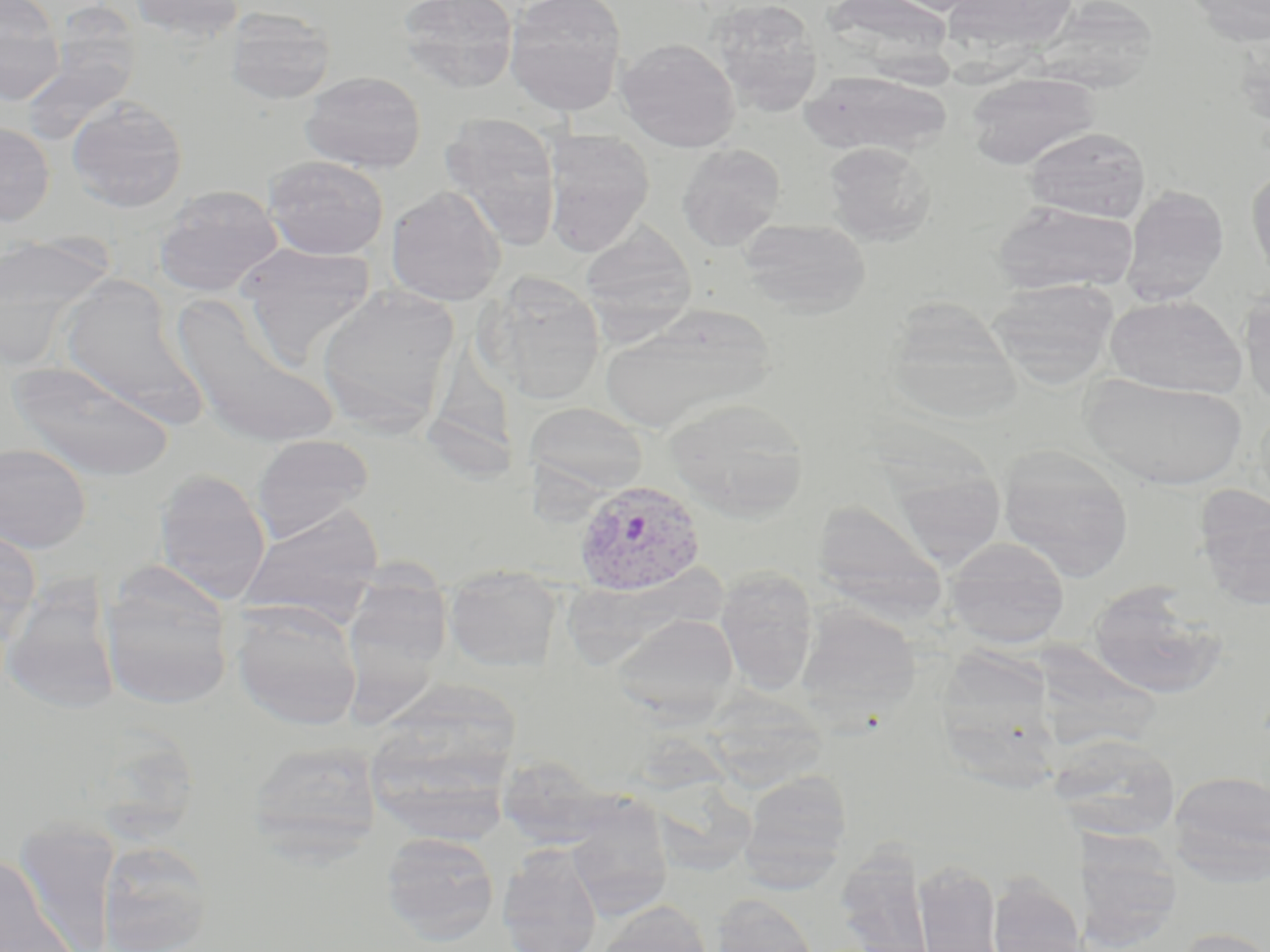
slide-level diagnosis = Plasmodium vivax
preparation = thin blood film
uninfected red blood cell locations = approximate bounding boxes as named x1/y1/x2/y2 corners in pixels: (x1=127, y1=0, x2=246, y2=41), (x1=396, y1=0, x2=519, y2=93), (x1=505, y1=0, x2=627, y2=115), (x1=710, y1=0, x2=823, y2=116), (x1=821, y1=0, x2=956, y2=72), (x1=942, y1=0, x2=1077, y2=53), (x1=1184, y1=0, x2=1270, y2=45), (x1=1034, y1=3, x2=1159, y2=92), (x1=224, y1=8, x2=336, y2=105), (x1=0, y1=11, x2=64, y2=106), (x1=20, y1=29, x2=141, y2=145), (x1=1232, y1=30, x2=1270, y2=133), (x1=616, y1=38, x2=740, y2=152), (x1=801, y1=70, x2=950, y2=156), (x1=301, y1=71, x2=425, y2=173), (x1=966, y1=72, x2=1099, y2=170), (x1=66, y1=96, x2=188, y2=212), (x1=440, y1=114, x2=563, y2=250), (x1=0, y1=123, x2=55, y2=225), (x1=1024, y1=126, x2=1151, y2=222), (x1=541, y1=130, x2=655, y2=255), (x1=824, y1=142, x2=934, y2=245), (x1=677, y1=144, x2=785, y2=250), (x1=263, y1=156, x2=389, y2=260), (x1=1246, y1=167, x2=1270, y2=286), (x1=153, y1=185, x2=283, y2=297), (x1=386, y1=185, x2=506, y2=306), (x1=1120, y1=185, x2=1229, y2=306), (x1=993, y1=201, x2=1139, y2=295), (x1=739, y1=218, x2=871, y2=316), (x1=580, y1=223, x2=697, y2=332), (x1=0, y1=231, x2=111, y2=349), (x1=238, y1=243, x2=377, y2=362), (x1=483, y1=277, x2=606, y2=405), (x1=986, y1=278, x2=1120, y2=387), (x1=57, y1=281, x2=204, y2=423), (x1=316, y1=284, x2=460, y2=434), (x1=1239, y1=289, x2=1270, y2=410), (x1=170, y1=292, x2=338, y2=450), (x1=1104, y1=295, x2=1246, y2=398), (x1=600, y1=305, x2=773, y2=434), (x1=901, y1=306, x2=1027, y2=431), (x1=429, y1=349, x2=527, y2=501), (x1=6, y1=358, x2=175, y2=481), (x1=1084, y1=375, x2=1247, y2=488), (x1=666, y1=396, x2=810, y2=520), (x1=524, y1=402, x2=648, y2=497), (x1=251, y1=435, x2=374, y2=542), (x1=0, y1=442, x2=92, y2=553), (x1=998, y1=445, x2=1135, y2=581), (x1=887, y1=459, x2=1007, y2=572), (x1=153, y1=468, x2=271, y2=603), (x1=1194, y1=487, x2=1270, y2=610), (x1=814, y1=501, x2=947, y2=617), (x1=238, y1=504, x2=384, y2=625), (x1=0, y1=527, x2=41, y2=651), (x1=943, y1=537, x2=1070, y2=648), (x1=352, y1=556, x2=458, y2=725), (x1=444, y1=565, x2=562, y2=672), (x1=715, y1=567, x2=819, y2=694), (x1=99, y1=570, x2=234, y2=711), (x1=2, y1=581, x2=119, y2=714), (x1=1087, y1=581, x2=1227, y2=700), (x1=230, y1=600, x2=363, y2=730), (x1=797, y1=604, x2=920, y2=723), (x1=610, y1=611, x2=739, y2=720), (x1=941, y1=639, x2=1059, y2=794), (x1=378, y1=677, x2=532, y2=841), (x1=713, y1=689, x2=833, y2=795), (x1=1048, y1=733, x2=1182, y2=841), (x1=247, y1=739, x2=383, y2=858), (x1=495, y1=757, x2=627, y2=850), (x1=738, y1=769, x2=854, y2=887), (x1=1168, y1=769, x2=1270, y2=884), (x1=566, y1=811, x2=672, y2=919), (x1=12, y1=822, x2=122, y2=951), (x1=1080, y1=828, x2=1182, y2=949), (x1=380, y1=831, x2=500, y2=946), (x1=95, y1=840, x2=216, y2=952), (x1=497, y1=844, x2=603, y2=952), (x1=836, y1=850, x2=936, y2=952), (x1=0, y1=854, x2=75, y2=952), (x1=914, y1=859, x2=1003, y2=952), (x1=987, y1=873, x2=1084, y2=952), (x1=709, y1=892, x2=821, y2=952), (x1=596, y1=900, x2=714, y2=952), (x1=1172, y1=926, x2=1270, y2=952)
image size = 1270×952 pixels
field of view = one of a larger specimen
Plasmodium vivax-infected red blood cell locations = approximate bounding boxes as named x1/y1/x2/y2 corners in pixels: (x1=572, y1=477, x2=707, y2=596)
modality = optical microscopy
stain = May-Grünwald-Giemsa
magnification = 1000x